Classify this cell by malaria status.
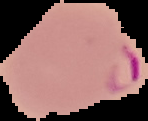

It is parasitized.

The area outside the segmented cell region is set to black. From a thin blood smear. Image is 148×121 pixels.